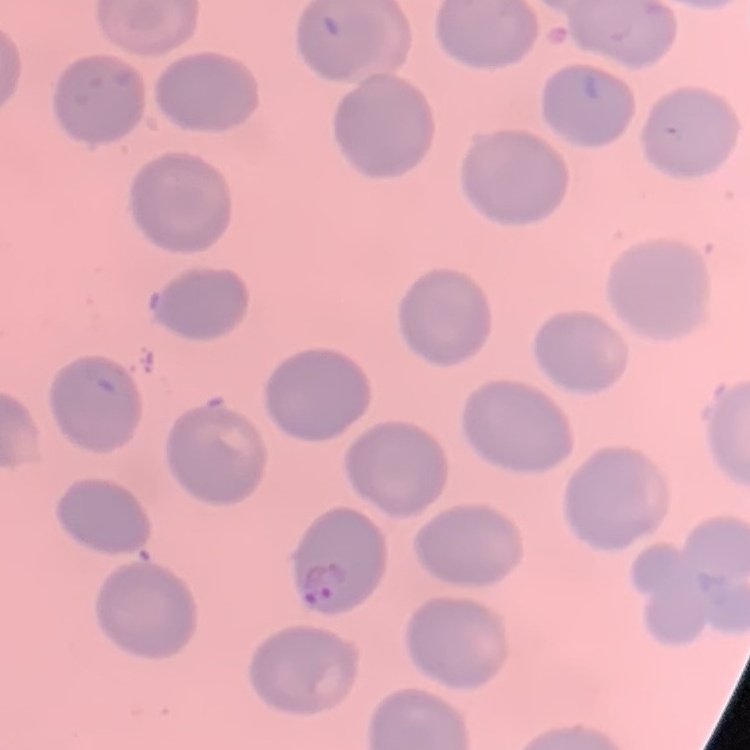
Summary:
  - Erythrocyte morphology: no rouleaux formation
  - Image type: square crop of a larger photomicrograph
  - Preparation: thin blood film
  - Stain: Field's or Giemsa